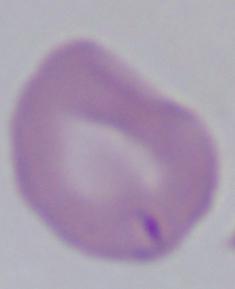

identification: Babesia
modality: photomicrograph
magnification: 1000x